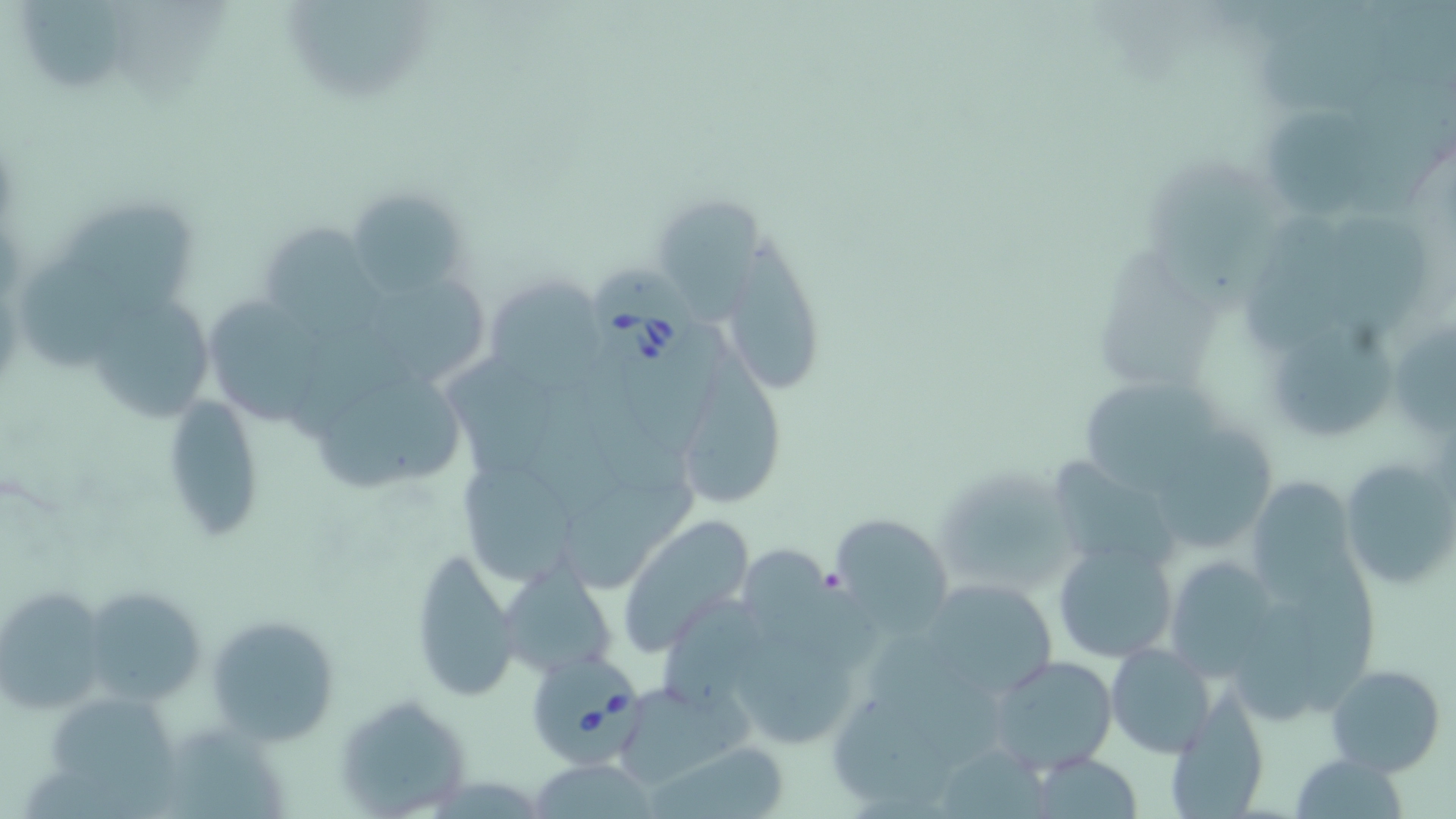
slide-level diagnosis = Babesia divergens
stain = May-Grünwald-Giemsa
field of view = one of a larger specimen
Babesia divergens-infected red blood cell locations = approximate bounding boxes as (x1, y1, x2, y2) in pixels: (592, 265, 695, 368), (524, 655, 649, 771)
image size = 1456×819 pixels
modality = light microscopy
preparation = thin blood smear
uninfected red blood cell locations = approximate bounding boxes as (x1, y1, x2, y2) in pixels: (15, 0, 131, 100), (1357, 71, 1456, 215), (1266, 109, 1383, 218), (1154, 163, 1285, 313), (345, 187, 473, 300), (659, 200, 771, 328), (70, 205, 202, 308), (1247, 207, 1357, 357), (1336, 218, 1432, 337), (265, 223, 399, 343), (728, 241, 830, 391), (1099, 250, 1222, 390), (24, 254, 127, 365), (491, 274, 615, 387), (366, 277, 495, 385), (97, 292, 211, 422), (209, 300, 324, 423), (1397, 322, 1456, 436), (1273, 328, 1400, 439), (684, 334, 793, 508), (456, 359, 564, 484), (584, 372, 691, 493), (321, 376, 467, 489), (535, 377, 623, 520), (1078, 379, 1242, 489), (160, 395, 265, 544), (1162, 426, 1280, 551), (1054, 453, 1189, 569), (1339, 456, 1454, 595), (466, 458, 574, 587), (935, 464, 1077, 597), (561, 478, 703, 584), (1252, 480, 1354, 597), (616, 513, 755, 655), (825, 513, 955, 630), (1052, 539, 1181, 666), (409, 546, 520, 702), (1301, 547, 1384, 716), (753, 554, 883, 668), (1165, 561, 1273, 682), (500, 564, 617, 679), (915, 575, 1063, 704), (78, 585, 206, 708), (661, 586, 766, 704), (0, 590, 106, 719), (1235, 602, 1324, 727), (209, 613, 339, 746), (875, 634, 1011, 759), (740, 640, 862, 747), (1104, 641, 1217, 759), (985, 654, 1118, 775), (1325, 664, 1446, 776), (613, 680, 753, 788), (334, 692, 476, 816), (1162, 692, 1271, 818), (54, 696, 183, 801), (834, 696, 956, 808), (162, 723, 284, 819), (650, 741, 792, 818), (943, 747, 1053, 819), (1292, 751, 1408, 819), (1024, 753, 1142, 817), (526, 759, 662, 817)
magnification = 1000x